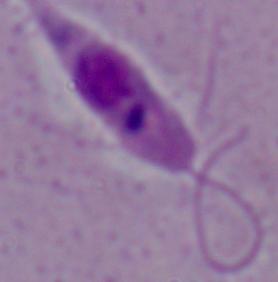

identification = Leishmania
modality = photomicrograph
magnification = 1000x